Locate every blood parasite and identify its species.
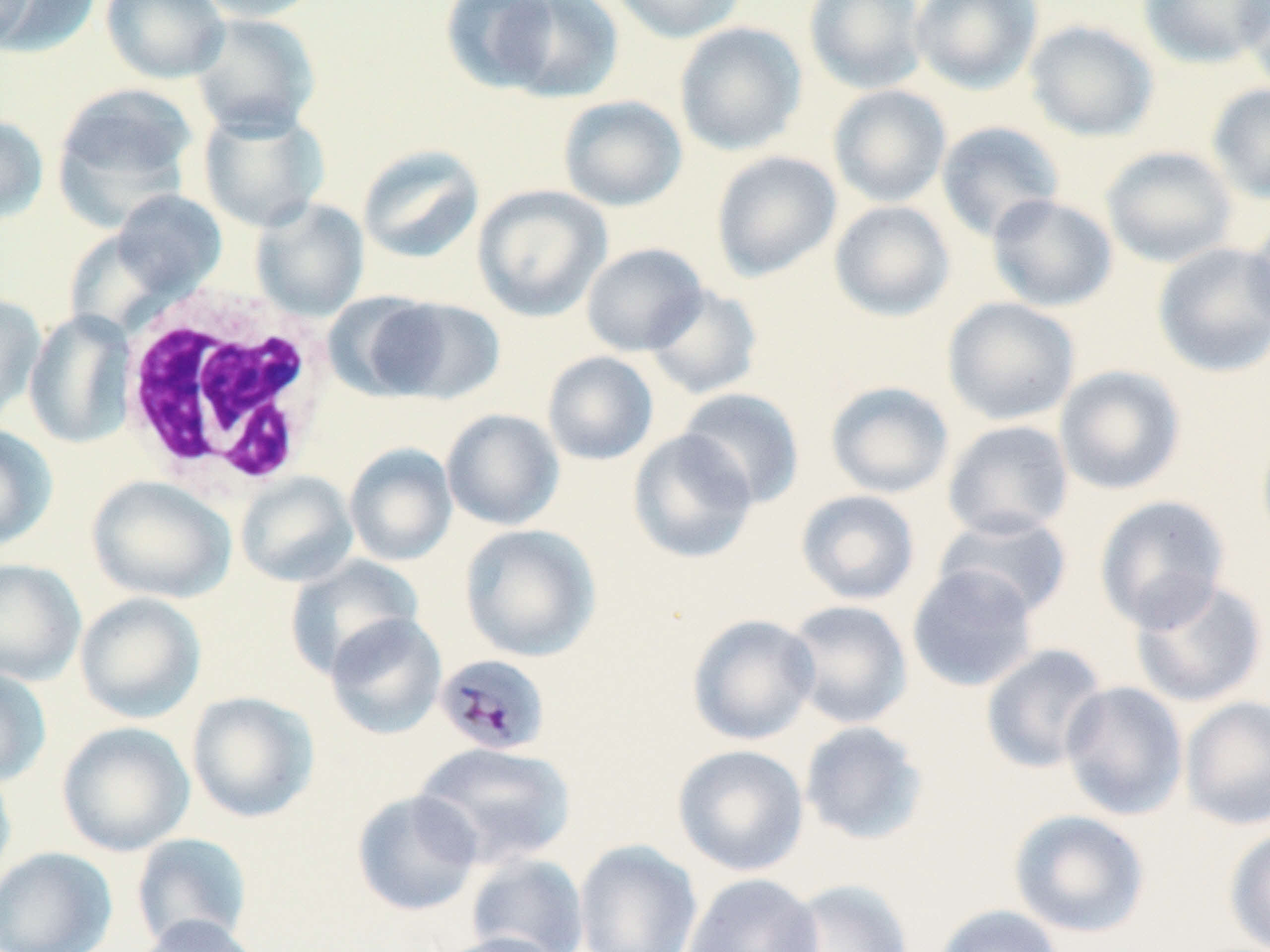
Approximate bounding boxes as (x1, y1, x2, y2) in pixels.
Plasmodium malariae-infected red blood cells: (434, 653, 551, 756).
No Plasmodium falciparum, Plasmodium ovale, Plasmodium vivax, Babesia divergens, or Trypanosoma brucei observed.

slide_level_diagnosis: Plasmodium malariae
modality: light microscopy
field_of_view: single
preparation: thin blood smear
white_blood_cell_locations: 'approximate bounding boxes as (x1, y1, x2, y2) in pixels: (114, 282, 340, 496)'
uninfected_red_blood_cell_locations: 'approximate bounding boxes as (x1, y1, x2, y2) in pixels: (2, 0, 102, 58), (100, 0, 230, 84), (190, 0, 326, 22), (440, 0, 563, 94), (608, 0, 749, 43), (803, 0, 929, 94), (909, 0, 1043, 93), (1138, 0, 1270, 69), (1237, 0, 1270, 94), (0, 1, 39, 51), (499, 1, 625, 103), (188, 12, 321, 138), (1024, 20, 1159, 142), (674, 22, 807, 156), (52, 83, 199, 224), (1207, 83, 1270, 204), (828, 84, 952, 208), (558, 96, 687, 212), (197, 105, 330, 233), (0, 113, 49, 225), (935, 120, 1065, 242), (357, 144, 485, 264), (1101, 146, 1238, 268), (710, 150, 842, 282), (472, 184, 613, 322), (110, 188, 227, 302), (986, 194, 1118, 313), (251, 198, 369, 321), (829, 200, 956, 322), (1245, 212, 1270, 338), (1152, 241, 1270, 378), (581, 242, 707, 356), (643, 283, 763, 400), (0, 292, 46, 424), (364, 295, 506, 404), (942, 296, 1081, 426), (24, 310, 135, 449), (542, 351, 659, 466), (1054, 365, 1186, 496), (825, 380, 954, 499), (677, 387, 805, 510), (441, 409, 564, 530), (942, 420, 1074, 540), (1256, 421, 1270, 548), (0, 424, 58, 552), (627, 428, 759, 565), (343, 443, 458, 567), (235, 472, 358, 588), (87, 475, 236, 604), (795, 489, 921, 605), (1094, 494, 1231, 632), (933, 512, 1074, 622), (459, 523, 602, 662), (285, 555, 425, 679), (0, 558, 86, 686), (907, 564, 1039, 693), (1130, 576, 1269, 708), (74, 591, 207, 724), (783, 599, 913, 729), (324, 612, 448, 740), (686, 613, 820, 746), (980, 643, 1108, 774), (0, 666, 52, 788), (1059, 680, 1189, 821), (186, 690, 320, 824), (1180, 695, 1270, 831), (799, 720, 929, 846), (56, 721, 195, 857), (413, 741, 578, 868), (672, 743, 809, 877), (0, 762, 17, 886), (351, 789, 482, 917), (1008, 809, 1151, 938), (1223, 826, 1270, 952), (130, 833, 253, 949), (574, 839, 703, 952), (0, 846, 117, 952), (465, 853, 590, 952), (682, 873, 824, 952), (779, 879, 914, 952), (934, 904, 1065, 952), (132, 914, 264, 952), (430, 931, 569, 952)'
stain: May-Grünwald-Giemsa
magnification: 1000x
image_size: 1270×952 pixels